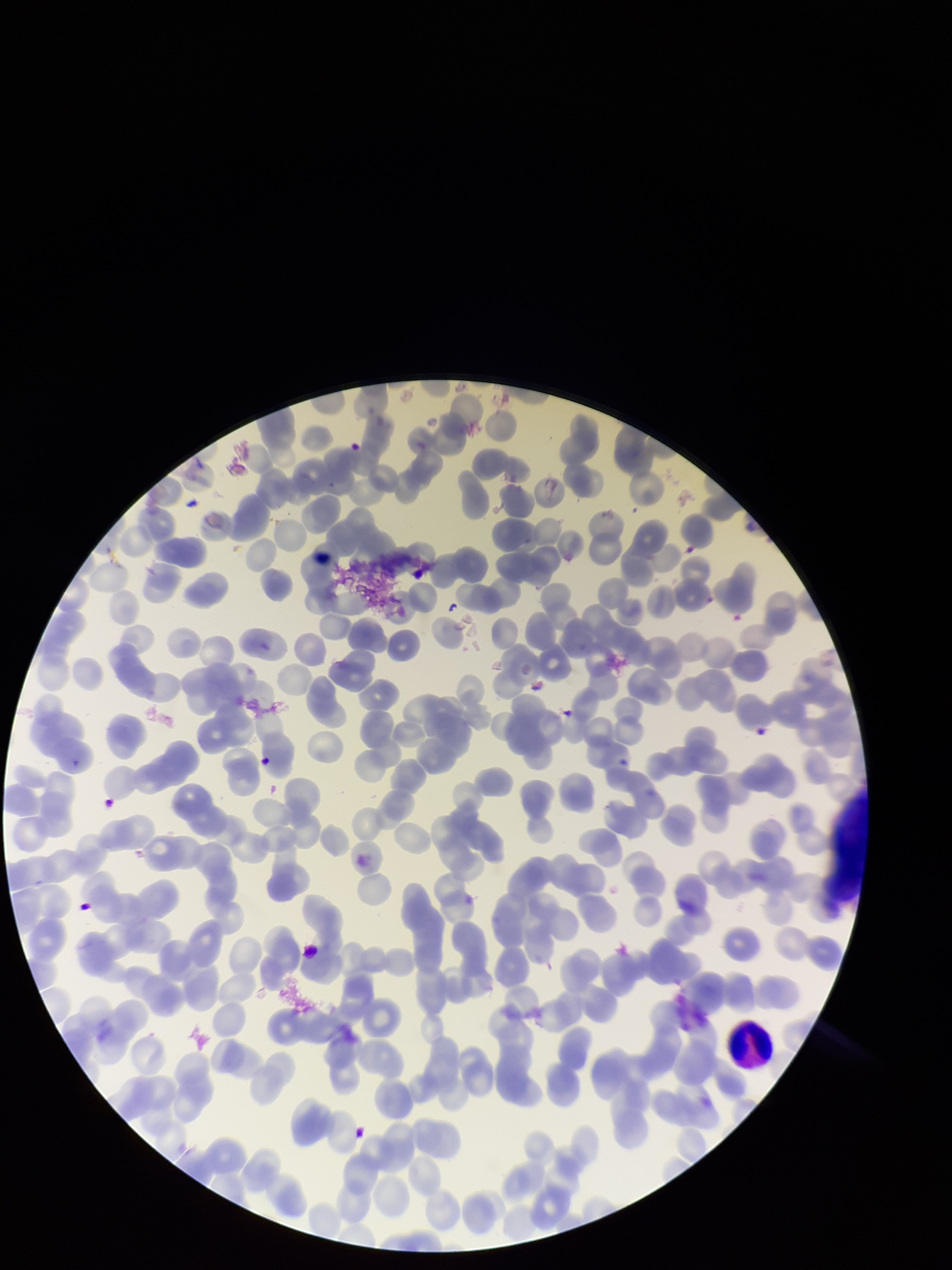

{
  "image_size": "952×1270 pixels",
  "capture": "smartphone photograph through the microscope eyepiece",
  "parasitized_red_blood_cells": "none detected",
  "stain": "Giemsa",
  "patient_malaria_status": "infected",
  "red_blood_cell_count": 227,
  "preparation": "thin",
  "parasitized_red_blood_cell_count": 0,
  "species_reported_for_this_patient": "Plasmodium falciparum",
  "field_of_view": "single"
}